Identify the blood parasite species.
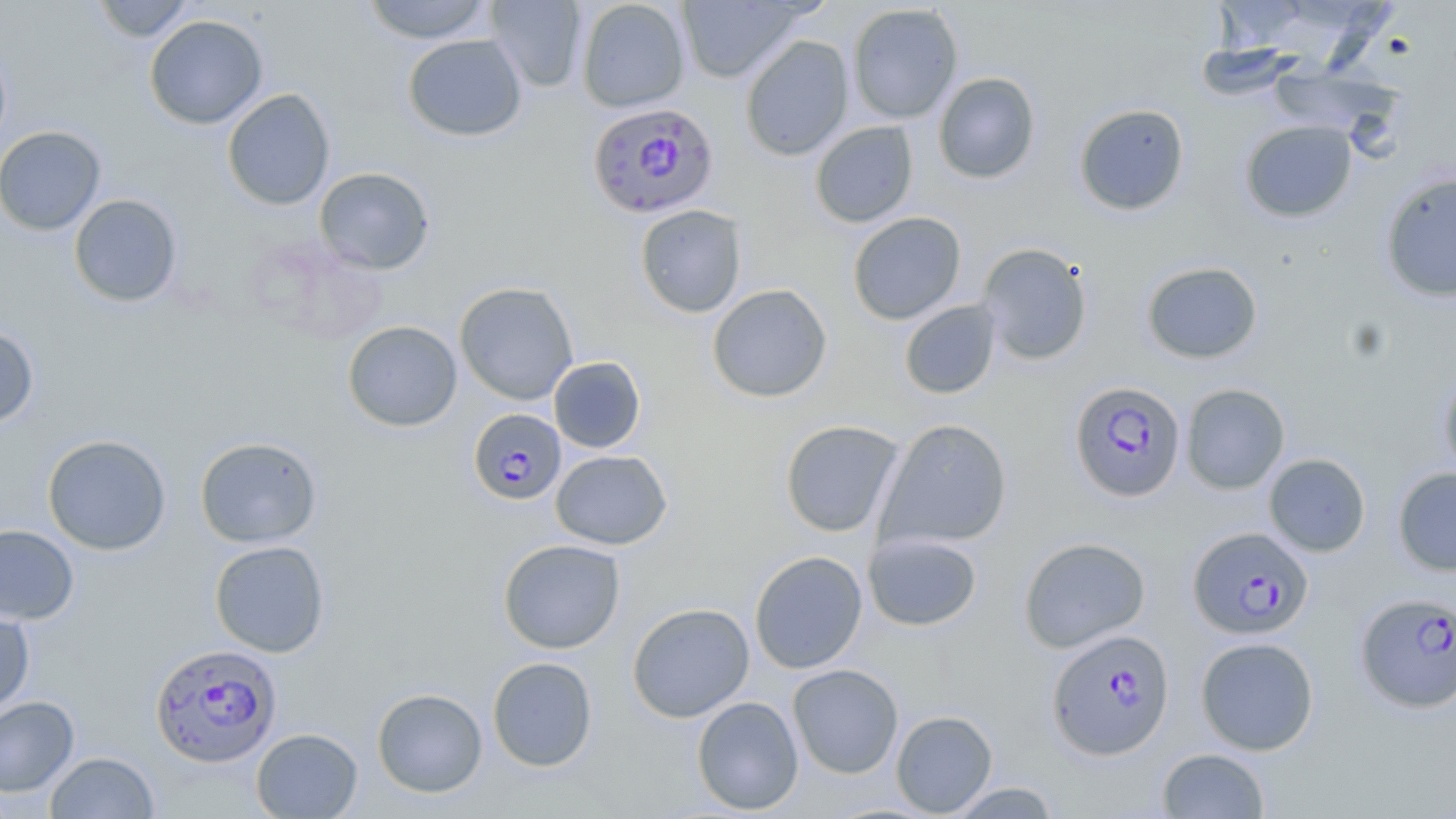

Plasmodium falciparum.

Approximate bounding boxes as [x1, y1, x2, y2] in pixels. Plasmodium falciparum-infected red blood cell locations: [587, 101, 719, 219], [1069, 380, 1186, 502], [468, 408, 567, 505], [1187, 526, 1313, 639], [1355, 591, 1456, 713], [1047, 628, 1175, 759], [150, 642, 281, 768]. Uninfected red blood cell locations: [92, 0, 196, 42], [362, 0, 492, 44], [485, 0, 587, 92], [577, 0, 690, 112], [676, 0, 807, 84], [1213, 0, 1312, 55], [847, 3, 964, 124], [144, 14, 268, 130], [402, 34, 527, 142], [740, 35, 854, 161], [0, 39, 12, 159], [1194, 43, 1299, 101], [1270, 64, 1400, 141], [933, 72, 1041, 184], [222, 88, 335, 211], [1074, 103, 1189, 216], [1240, 120, 1358, 222], [810, 121, 919, 228], [0, 125, 106, 236], [314, 167, 436, 274], [1380, 172, 1456, 302], [69, 194, 183, 307], [635, 204, 747, 318], [848, 212, 966, 325], [977, 242, 1093, 365], [1142, 261, 1263, 364], [454, 282, 579, 405], [707, 284, 833, 403], [899, 300, 1001, 399], [343, 320, 462, 431], [0, 324, 40, 429], [549, 356, 646, 453], [1439, 365, 1456, 483], [1181, 383, 1290, 494], [876, 417, 1013, 552], [779, 420, 905, 537], [42, 434, 171, 556], [195, 436, 322, 548], [551, 449, 672, 550], [1264, 453, 1370, 557], [1392, 467, 1456, 576], [0, 524, 80, 625], [863, 532, 983, 632], [1019, 536, 1151, 653], [498, 538, 625, 654], [209, 540, 330, 657], [749, 550, 868, 674], [628, 602, 755, 723], [0, 608, 35, 715], [1195, 636, 1319, 756], [487, 656, 598, 772], [787, 664, 904, 778], [372, 687, 488, 797], [0, 696, 80, 797], [691, 696, 804, 815], [891, 710, 998, 817], [251, 728, 363, 818], [1157, 748, 1270, 818], [46, 751, 159, 818], [946, 782, 1061, 818]. Thin blood smear. Single field of view. Captured at 1000x magnification. May-Grünwald-Giemsa stain. Image is 1456×819 pixels. Optical microscopy.